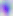

Summary:
  - Magnification: 400x
  - Identification: Toxoplasma gondii
  - Modality: photomicrograph